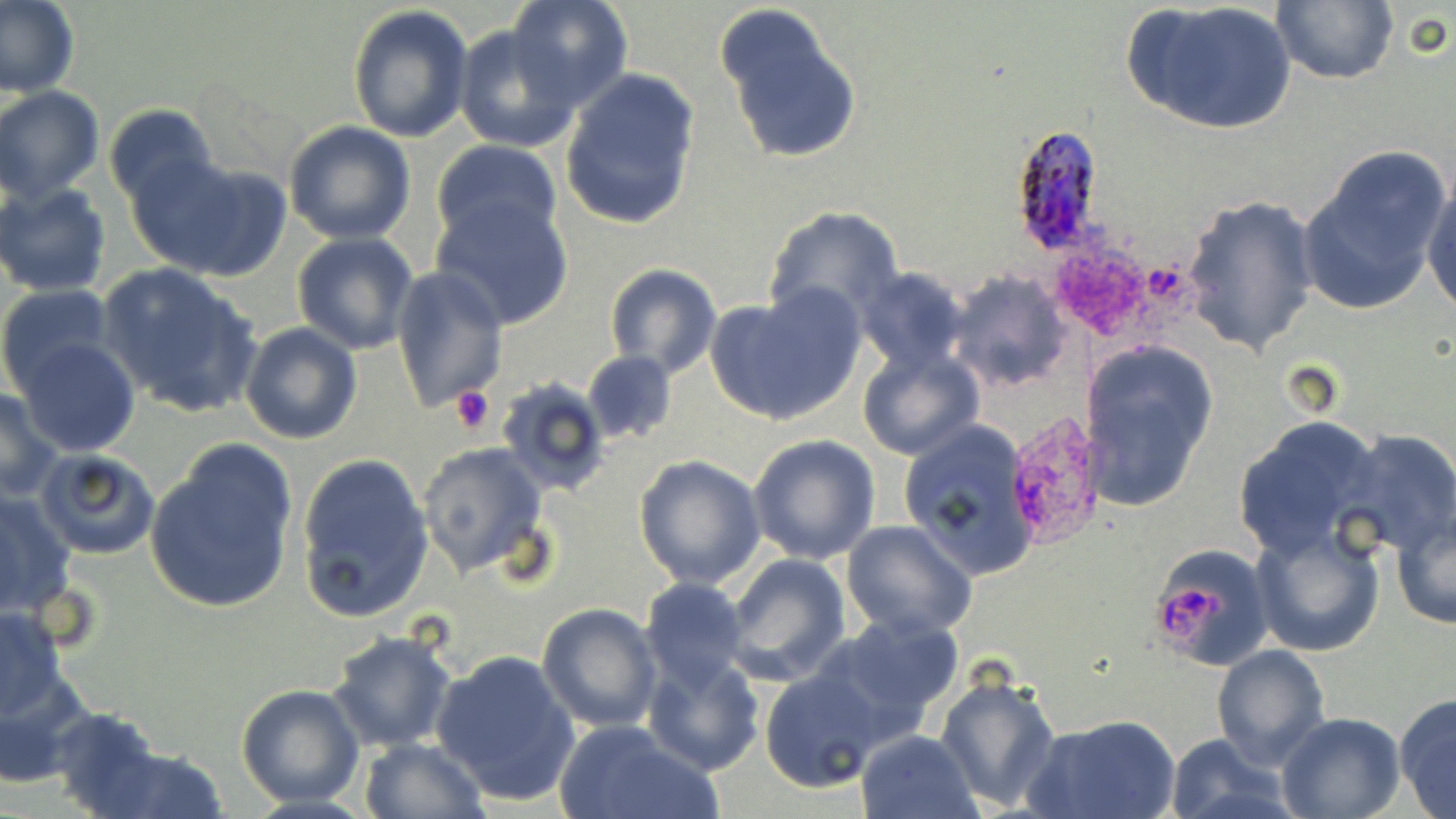

slide-level diagnosis = Plasmodium ovale
image size = 1456×819 pixels
modality = light microscopy
Plasmodium ovale-infected red blood cell locations = approximate bounding boxes as (x1, y1, x2, y2) in pixels: (1009, 125, 1109, 258)
stain = May-Grünwald-Giemsa
magnification = 1000x
uninfected red blood cell locations = approximate bounding boxes as (x1, y1, x2, y2) in pixels: (0, 0, 81, 100), (507, 0, 633, 108), (1124, 0, 1296, 137), (1270, 0, 1398, 86), (715, 2, 863, 166), (348, 5, 474, 144), (454, 22, 585, 152), (558, 68, 701, 231), (0, 86, 104, 202), (104, 104, 218, 210), (284, 119, 417, 244), (431, 139, 563, 247), (1296, 147, 1455, 314), (133, 153, 292, 283), (1423, 178, 1456, 317), (1, 181, 112, 298), (1182, 193, 1321, 357), (431, 194, 575, 330), (762, 206, 907, 326), (291, 231, 419, 354), (97, 263, 263, 418), (605, 264, 722, 379), (389, 266, 509, 412), (854, 267, 971, 375), (946, 270, 1071, 394), (0, 283, 116, 394), (706, 287, 864, 424), (238, 322, 362, 444), (14, 339, 140, 456), (1081, 341, 1217, 512), (856, 345, 985, 461), (582, 349, 677, 445), (496, 375, 612, 498), (0, 386, 65, 501), (1233, 416, 1387, 560), (899, 420, 1040, 581), (1341, 431, 1455, 557), (748, 433, 880, 564), (415, 442, 550, 580), (146, 443, 300, 615), (34, 448, 163, 561), (296, 451, 435, 623), (633, 454, 766, 591), (0, 489, 76, 617), (1390, 506, 1455, 633), (841, 520, 979, 640), (1251, 521, 1386, 657), (1148, 544, 1271, 668), (723, 554, 852, 685), (640, 577, 752, 693), (537, 601, 662, 732), (0, 604, 67, 718), (817, 614, 964, 738), (326, 630, 459, 753), (1209, 644, 1331, 771), (430, 648, 580, 806), (641, 652, 764, 775), (0, 665, 97, 788), (759, 669, 884, 793), (935, 671, 1061, 811), (236, 683, 365, 808), (1393, 693, 1456, 819), (47, 708, 170, 819), (1274, 712, 1404, 819), (1029, 713, 1179, 819), (553, 719, 723, 819), (856, 729, 982, 819), (1163, 733, 1294, 819), (359, 737, 489, 819), (80, 743, 231, 818)
field of view = one of a larger specimen
preparation = thin blood film
platelet locations = approximate bounding boxes as (x1, y1, x2, y2) in pixels: (1045, 234, 1161, 344), (447, 384, 499, 437), (1164, 587, 1218, 640)